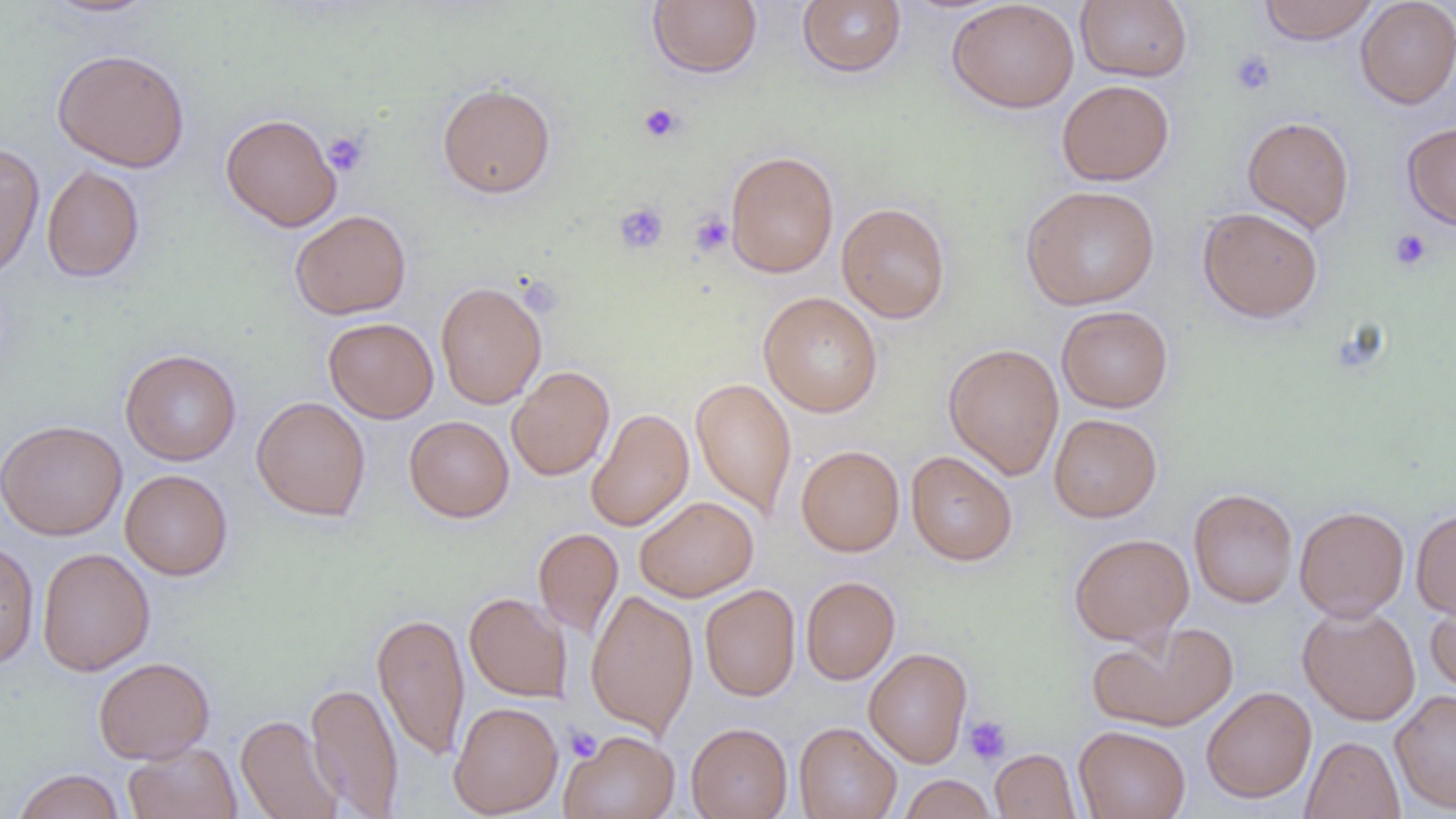

Approximate bounding boxes as named x1/y1/x2/y2 corners in pixels. Uninfected red blood cell locations: (x1=38, y1=0, x2=160, y2=18), (x1=648, y1=0, x2=763, y2=78), (x1=946, y1=0, x2=1080, y2=113), (x1=1075, y1=0, x2=1193, y2=82), (x1=1258, y1=0, x2=1380, y2=44), (x1=1355, y1=0, x2=1456, y2=109), (x1=797, y1=1, x2=906, y2=77), (x1=51, y1=48, x2=190, y2=173), (x1=1057, y1=79, x2=1174, y2=186), (x1=437, y1=82, x2=556, y2=199), (x1=220, y1=113, x2=342, y2=232), (x1=1242, y1=115, x2=1355, y2=232), (x1=1402, y1=121, x2=1456, y2=231), (x1=0, y1=142, x2=45, y2=283), (x1=724, y1=150, x2=839, y2=278), (x1=41, y1=164, x2=145, y2=283), (x1=1021, y1=185, x2=1160, y2=310), (x1=836, y1=202, x2=951, y2=323), (x1=1197, y1=206, x2=1324, y2=322), (x1=290, y1=210, x2=411, y2=319), (x1=435, y1=280, x2=547, y2=409), (x1=758, y1=292, x2=883, y2=417), (x1=1056, y1=305, x2=1173, y2=413), (x1=323, y1=317, x2=438, y2=423), (x1=943, y1=343, x2=1064, y2=480), (x1=120, y1=349, x2=241, y2=465), (x1=507, y1=366, x2=614, y2=481), (x1=690, y1=378, x2=797, y2=520), (x1=251, y1=396, x2=371, y2=521), (x1=586, y1=407, x2=694, y2=532), (x1=1049, y1=413, x2=1162, y2=522), (x1=404, y1=416, x2=514, y2=522), (x1=0, y1=419, x2=127, y2=540), (x1=796, y1=445, x2=905, y2=556), (x1=906, y1=450, x2=1018, y2=566), (x1=120, y1=469, x2=233, y2=580), (x1=1188, y1=488, x2=1298, y2=607), (x1=635, y1=496, x2=759, y2=602), (x1=1294, y1=505, x2=1409, y2=621), (x1=1411, y1=508, x2=1456, y2=620), (x1=533, y1=528, x2=624, y2=640), (x1=1069, y1=532, x2=1193, y2=646), (x1=0, y1=539, x2=39, y2=671), (x1=37, y1=547, x2=155, y2=676), (x1=801, y1=576, x2=900, y2=684), (x1=700, y1=583, x2=801, y2=701), (x1=585, y1=589, x2=699, y2=738), (x1=464, y1=592, x2=572, y2=702), (x1=1424, y1=595, x2=1456, y2=696), (x1=1297, y1=604, x2=1421, y2=726), (x1=372, y1=611, x2=470, y2=760), (x1=1087, y1=620, x2=1238, y2=733), (x1=863, y1=648, x2=973, y2=767), (x1=93, y1=656, x2=215, y2=763), (x1=305, y1=680, x2=404, y2=818), (x1=1201, y1=686, x2=1317, y2=803), (x1=1390, y1=688, x2=1456, y2=813), (x1=449, y1=701, x2=563, y2=818), (x1=236, y1=714, x2=344, y2=819), (x1=686, y1=722, x2=793, y2=819), (x1=794, y1=722, x2=902, y2=819), (x1=1073, y1=725, x2=1191, y2=819), (x1=561, y1=729, x2=679, y2=818), (x1=1301, y1=736, x2=1405, y2=819), (x1=124, y1=742, x2=242, y2=819), (x1=990, y1=748, x2=1081, y2=818), (x1=11, y1=768, x2=126, y2=819), (x1=898, y1=774, x2=996, y2=818). Platelet locations: (x1=1229, y1=49, x2=1276, y2=96), (x1=639, y1=103, x2=683, y2=143), (x1=322, y1=130, x2=370, y2=177), (x1=614, y1=201, x2=668, y2=255), (x1=689, y1=212, x2=733, y2=258), (x1=1389, y1=228, x2=1432, y2=271), (x1=964, y1=715, x2=1012, y2=766), (x1=565, y1=726, x2=602, y2=762). Slide-level diagnosis: no evidence of blood parasites. One field of a larger specimen. Thin blood film. Optical microscopy. 1000x magnification. Image is 1456×819 pixels.